Assess this cell for malaria.
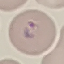
It is parasitized.

Giemsa stain. Thin blood film. Acquired by smartphone through the microscope eyepiece. Cell patch, automatically extracted from a larger field of view and resized to 64 × 64 pixels.